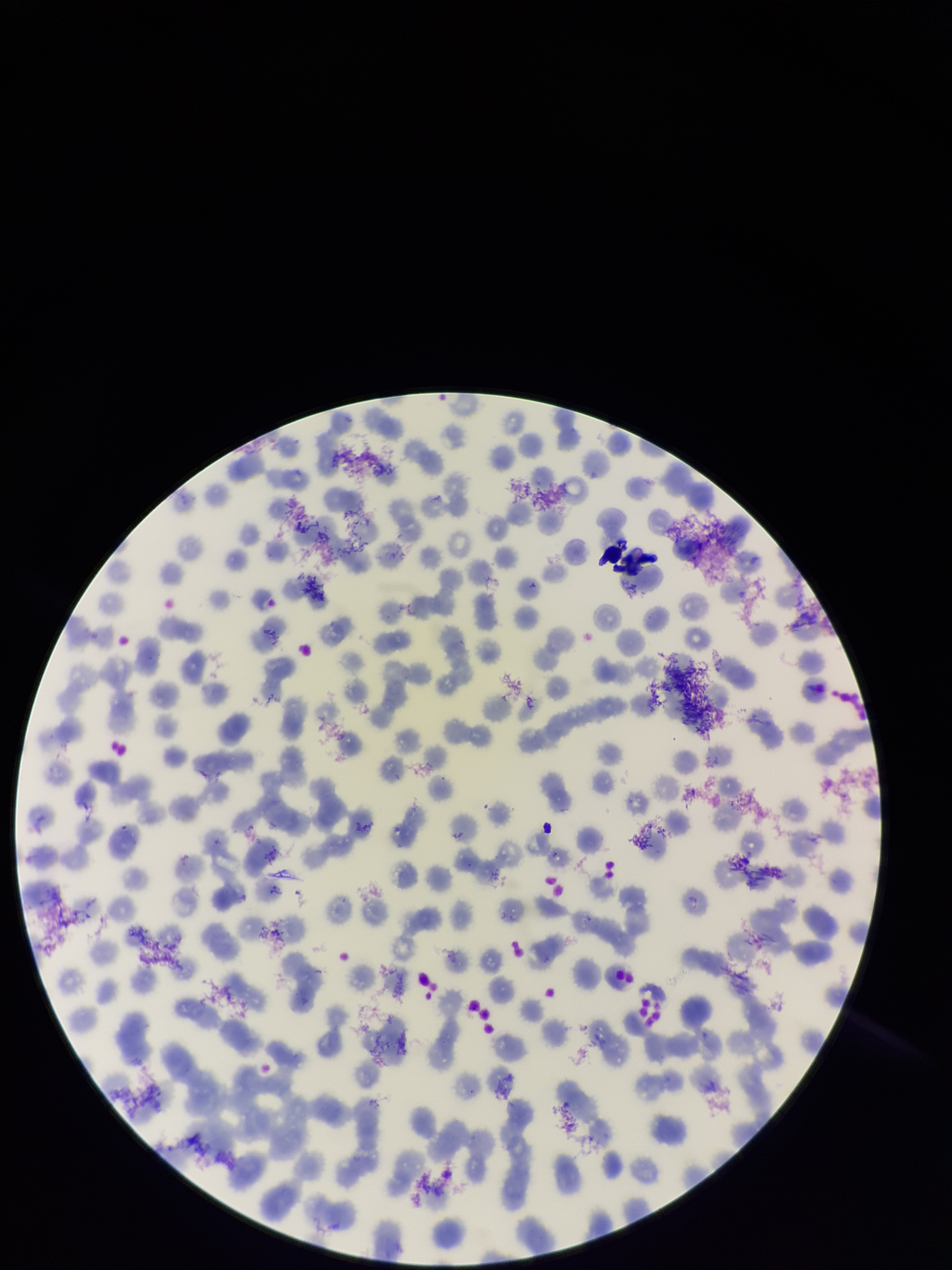
field of view = single
red blood cell count = 293
preparation = thin smear
patient malaria status = negative
parasitized red blood cells = none detected
capture = smartphone photograph through the microscope eyepiece
image size = 952×1270 pixels
parasitized red blood cell count = 0
stain = Giemsa